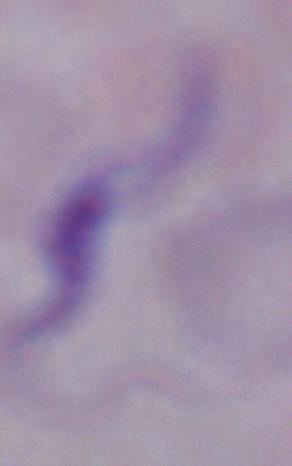

Summary:
  - Modality: micrograph
  - Magnification: 1000x
  - Identification: trypanosome